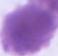 Captured at 1000x magnification. Micrograph. A red blood cell is seen.